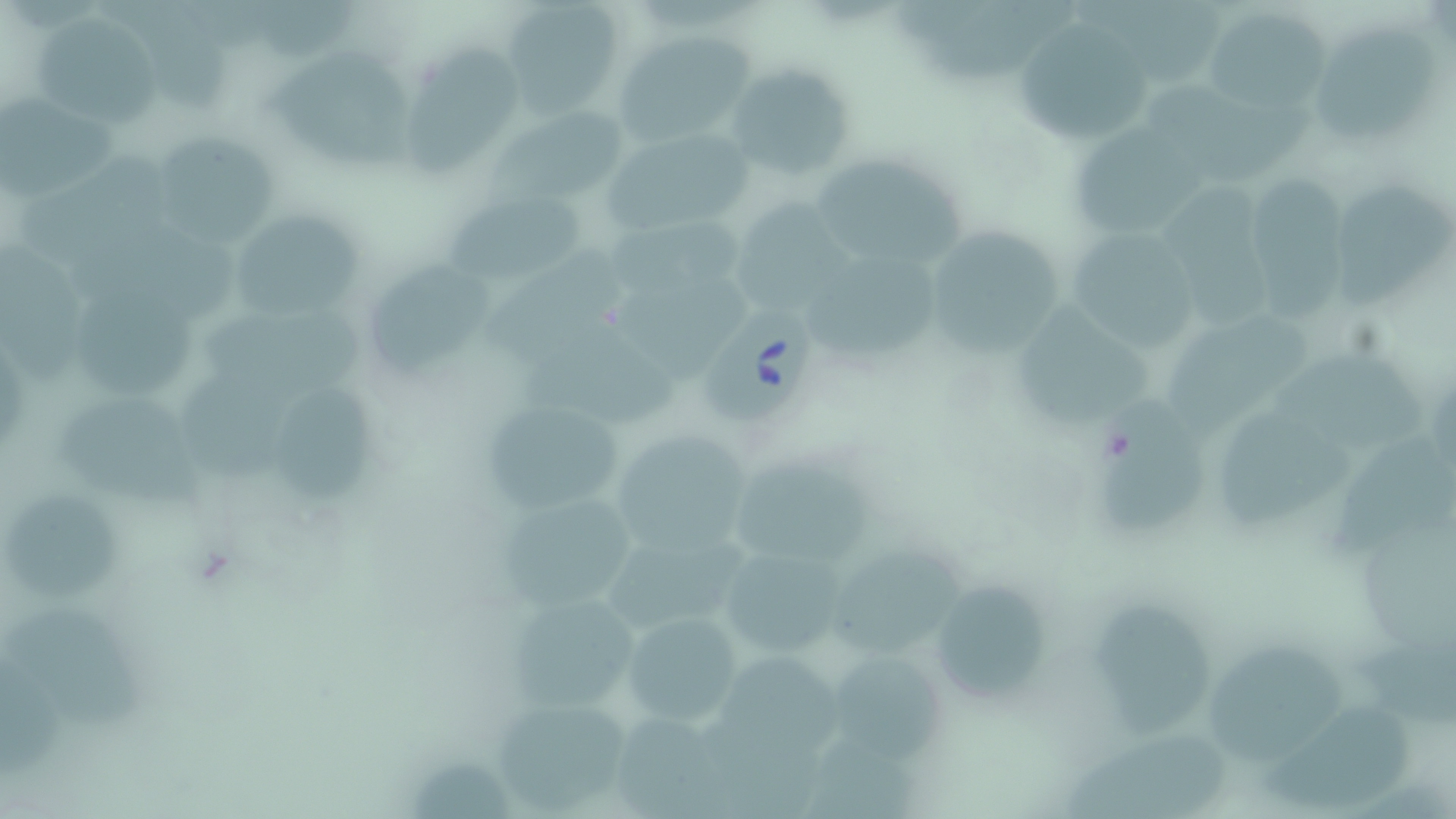
Summary:
  - Coordinate format: approximate bounding boxes as [x1, y1, x2, y2] in pixels
  - Babesia divergens-infected red blood cell locations: [703, 300, 820, 424]
  - Uninfected red blood cell locations: [1075, 0, 1222, 89], [503, 1, 626, 116], [1201, 7, 1328, 115], [36, 14, 157, 128], [1009, 18, 1152, 143], [1311, 22, 1439, 142], [613, 33, 752, 145], [411, 42, 520, 176], [269, 51, 417, 173], [728, 63, 856, 184], [1153, 75, 1315, 181], [1, 95, 122, 204], [1068, 124, 1209, 235], [614, 130, 747, 232], [156, 134, 278, 248], [811, 149, 968, 276], [1251, 171, 1346, 320], [1333, 174, 1455, 315], [1165, 180, 1280, 332], [447, 195, 583, 289], [743, 202, 854, 318], [602, 212, 751, 294], [232, 215, 361, 319], [922, 225, 1068, 353], [1069, 228, 1198, 354], [1, 234, 85, 382], [487, 241, 623, 355], [805, 256, 940, 365], [373, 260, 494, 380], [617, 272, 755, 377], [77, 283, 200, 400], [201, 299, 378, 402], [1015, 299, 1153, 429], [1163, 313, 1312, 429], [518, 322, 683, 430], [1275, 344, 1431, 452], [181, 367, 306, 487], [59, 389, 213, 514], [272, 391, 375, 503], [1096, 392, 1214, 539], [480, 395, 628, 521], [1221, 407, 1357, 529], [607, 429, 753, 558], [1332, 431, 1456, 552], [732, 460, 873, 562], [491, 487, 647, 610], [7, 492, 120, 602], [719, 541, 852, 666], [833, 547, 965, 660], [932, 572, 1044, 703], [501, 590, 642, 717], [1091, 601, 1201, 737], [3, 607, 145, 730], [624, 612, 744, 730], [1208, 645, 1336, 764], [725, 650, 850, 764], [828, 657, 944, 756], [2, 658, 67, 779], [490, 692, 637, 813], [1262, 704, 1412, 809], [1060, 731, 1235, 819]
  - Slide-level diagnosis: Babesia divergens
  - Field of view: one of a larger specimen
  - Image size: 1456×819 pixels
  - Magnification: 1000x
  - Preparation: thin blood film
  - Stain: May-Grünwald-Giemsa
  - Modality: light microscopy